Classify this cell by malaria status.
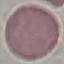
It is uninfected.

{
  "preparation": "thin blood smear",
  "image_type": "cell patch, automatically extracted from a larger field of view and resized to 64 × 64 pixels",
  "stain": "Giemsa",
  "capture": "smartphone through the microscope eyepiece"
}